Report the malaria status.
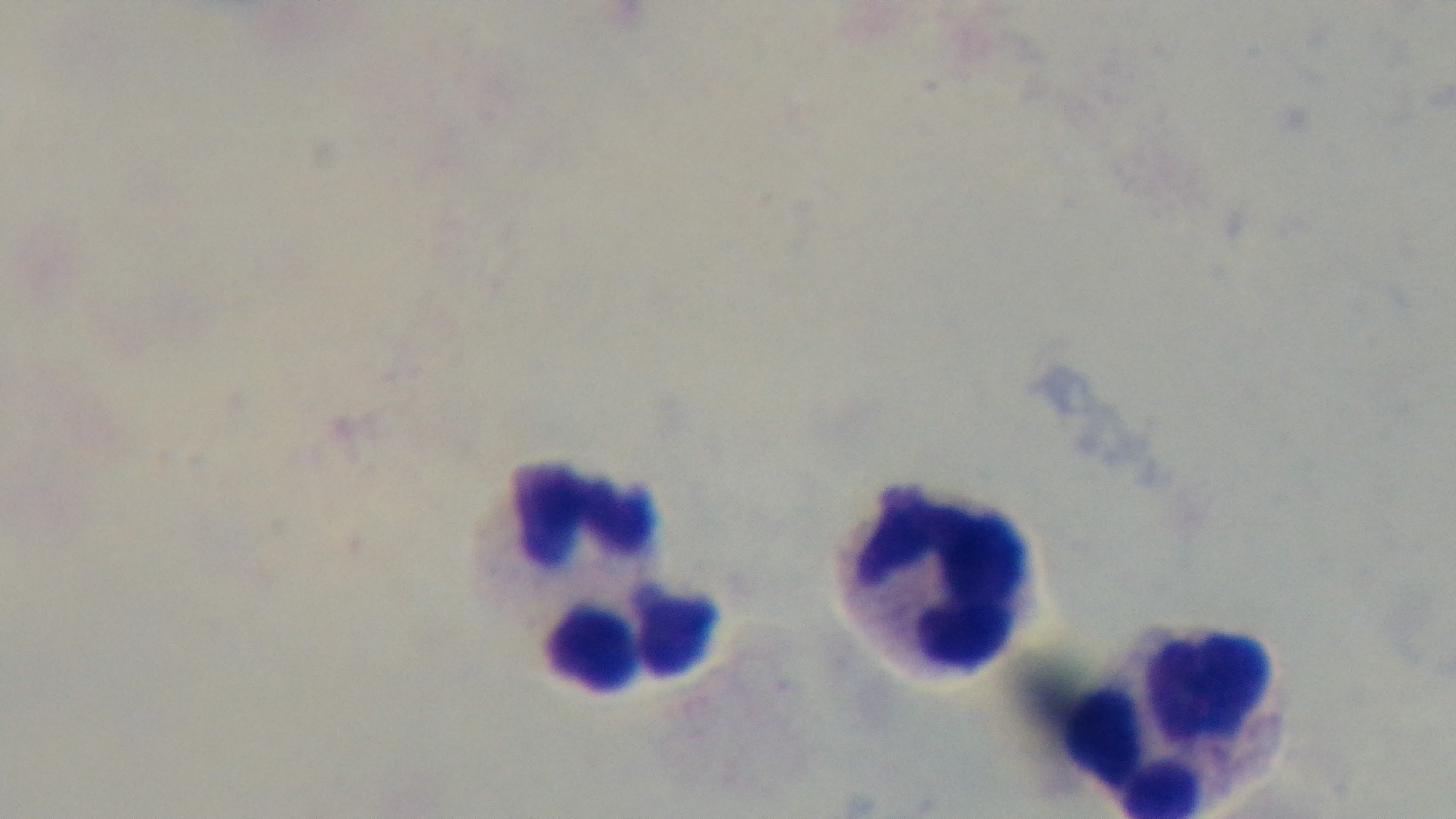

It is uninfected.

{
  "modality": "light microscopy",
  "stain": "Giemsa",
  "preparation": "thick smear",
  "capture": "mounted 4K digital camera",
  "objective": "100x oil immersion",
  "field_of_view": "one from the slide"
}